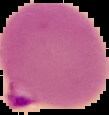
Summary:
  - Result: Plasmodium parasites identified
  - Preparation: thin blood film
  - Image size: 109×115 pixels
  - Image type: segmented cell region on a black background